Assess the morphology of the erythrocytes.
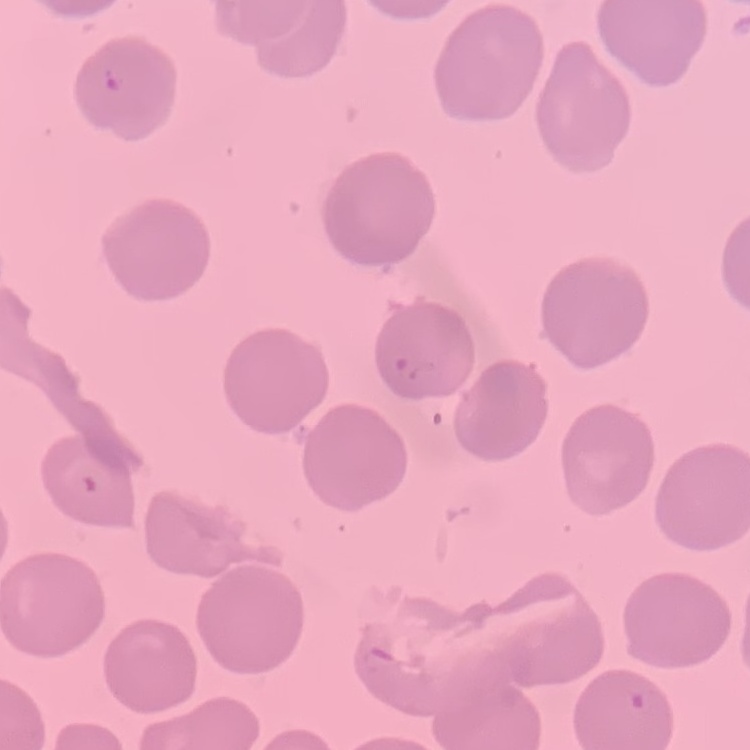
No rouleaux formation.

One tile cut from a larger photomicrograph. Thin blood smear. Stained with either Field's or Giemsa.